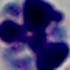
Summary:
  - Modality: micrograph
  - Identification: white blood cell
  - Magnification: 1000x